Identify the parasite.
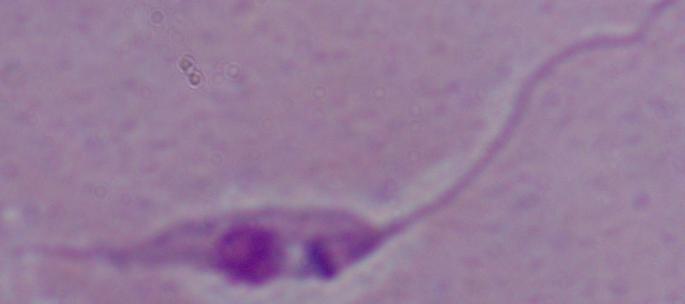
This is Leishmania.

Summary:
  - Magnification: 1000x
  - Modality: micrograph